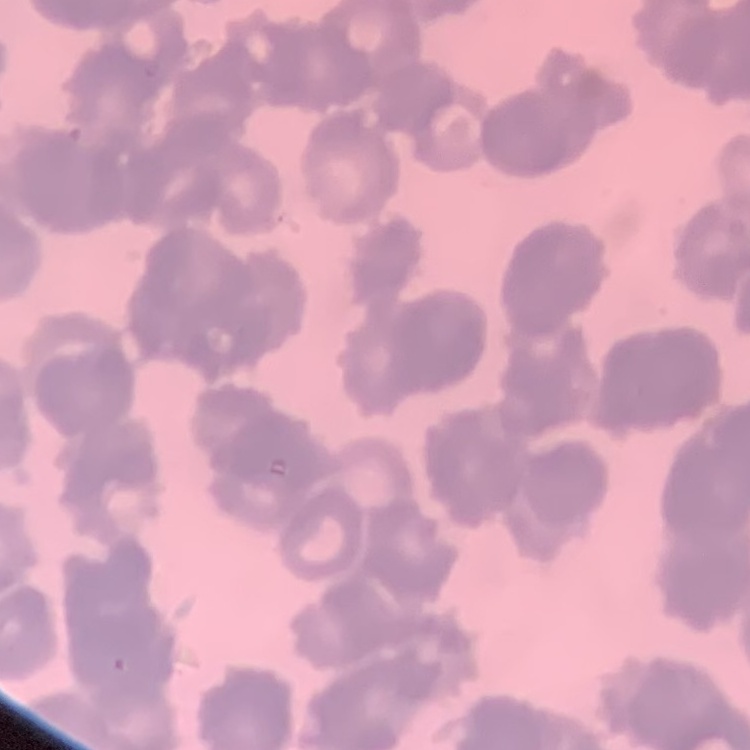

{
  "red_blood_cell_morphology": "rouleaux formation",
  "image_type": "square crop of a larger photomicrograph",
  "preparation": "thin peripheral smear",
  "stain": "Field's or Giemsa"
}